Classify this cell by malaria status.
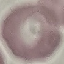
Uninfected.

Summary:
  - Preparation: thin blood smear
  - Image type: automatically extracted cell patch, resized to 64 × 64 pixels
  - Capture: smartphone camera at the microscope eyepiece
  - Stain: Giemsa